Classify this cell by malaria status.
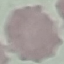

Uninfected.

Acquired by smartphone through the microscope eyepiece. Cell patch, automatically extracted from a larger field of view and resized to 64 × 64 pixels. Giemsa stain. Thin smear of blood.